Find each WBC.
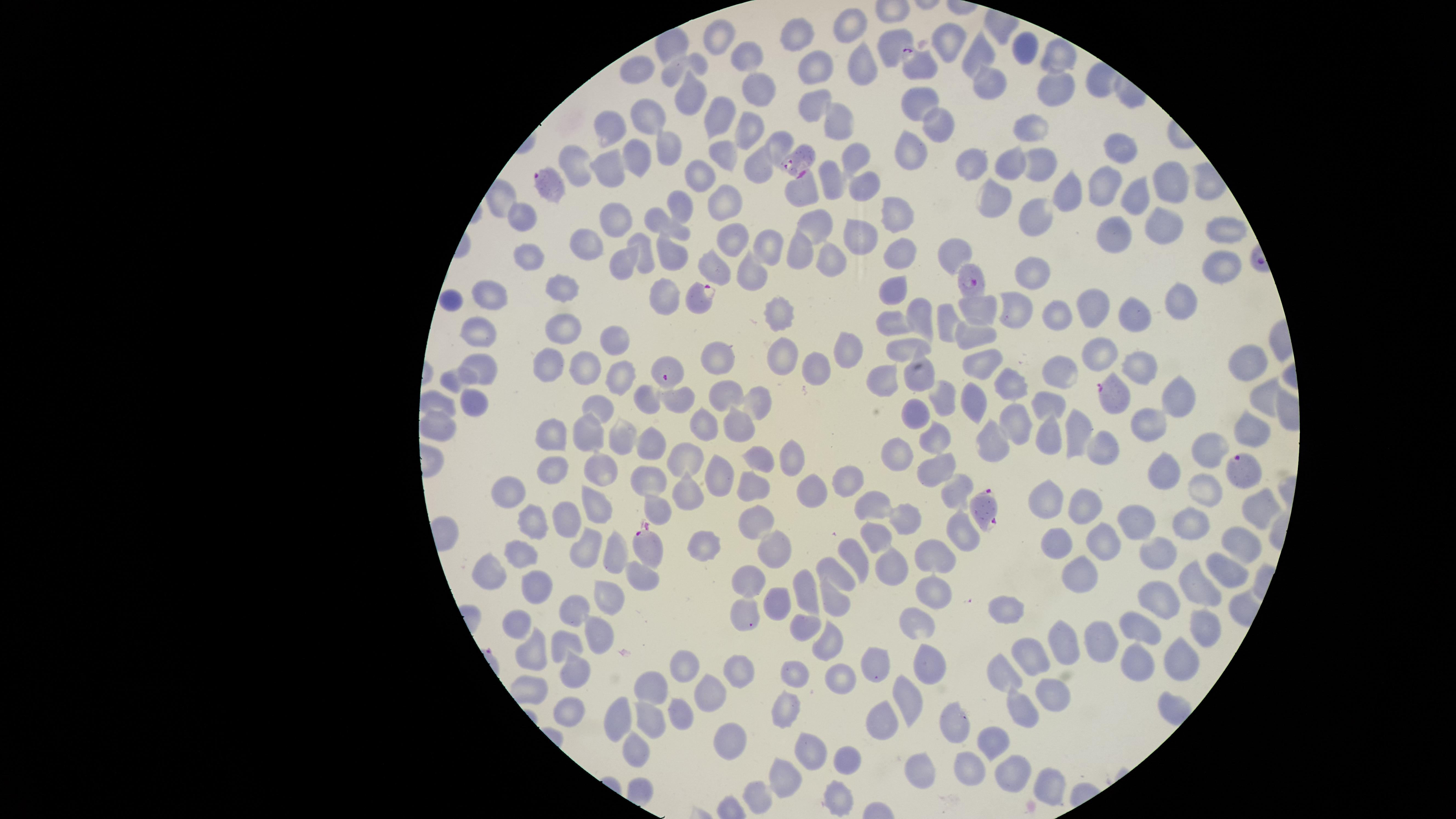
No WBCs identified.

image size = 1456×819 pixels
presence = malaria parasites identified
visible region = circular
stain = Giemsa
field of view = single
preparation = thin blood film
parasitized RBCs = approximate marker points as (x, y) in pixels: (924, 66), (799, 158), (549, 181), (966, 278), (698, 295), (665, 371), (1112, 393), (1242, 467), (985, 506), (645, 547)
uninfected RBCs = approximate marker points as (x, y) in pixels: (849, 25), (796, 30), (718, 35), (948, 37), (894, 39), (1017, 48), (978, 53), (1058, 53), (742, 56), (858, 62), (638, 70), (672, 72), (815, 72), (988, 84), (755, 89), (1055, 90), (690, 95), (920, 100), (810, 103), (645, 112), (715, 116), (838, 122), (933, 125), (748, 126), (611, 128), (1033, 131), (666, 143), (777, 144), (1118, 145), (911, 151), (721, 155), (633, 157), (856, 157), (1010, 161), (1039, 163), (973, 164), (580, 167), (611, 169), (756, 169), (699, 174), (831, 174), (1165, 180), (863, 185), (1103, 187), (802, 188), (1064, 194), (994, 198), (723, 199), (1132, 199), (680, 203), (896, 217), (523, 218), (1032, 219), (612, 225), (666, 226), (1160, 226), (818, 228), (1221, 228), (1109, 232), (732, 236), (857, 239), (769, 241), (586, 244), (795, 247), (642, 251), (899, 251), (672, 255), (954, 256), (528, 257), (827, 260), (714, 263), (625, 265), (1221, 267), (752, 273), (1030, 273), (566, 286), (892, 289), (493, 297), (451, 301), (665, 302), (1179, 303), (1092, 307), (780, 311), (978, 313), (1015, 313), (1133, 313), (921, 315), (1054, 315), (943, 321), (893, 323), (563, 328), (481, 332), (616, 333), (976, 334), (907, 347), (844, 349), (1097, 349), (783, 351), (717, 361), (819, 364), (550, 365), (1138, 365), (1247, 365), (585, 369), (981, 369), (1058, 369), (474, 372), (618, 376), (882, 378), (920, 378), (448, 380), (1003, 386), (726, 397), (942, 399), (1262, 399), (758, 400), (971, 400), (1176, 400), (643, 402), (676, 402), (1049, 403), (436, 404), (474, 410), (602, 410), (913, 416), (1016, 423), (1142, 423), (1078, 424), (697, 425), (436, 429), (741, 432), (1048, 432), (619, 433), (551, 435), (583, 435), (1248, 436), (939, 437), (650, 441), (1099, 442), (990, 445), (1201, 450), (792, 453), (897, 455), (683, 461), (762, 462), (601, 468), (557, 469), (1166, 470), (934, 472), (723, 473), (655, 480), (841, 480), (752, 487), (806, 487), (1204, 490), (505, 493), (688, 493), (956, 493), (1051, 497), (594, 503), (876, 503), (1080, 503), (657, 505), (1252, 507), (564, 515), (751, 515), (909, 518), (1137, 518), (1187, 525), (529, 527), (962, 535), (876, 537), (1059, 541), (1099, 541), (704, 542), (582, 543), (1240, 543), (775, 550), (1156, 551), (608, 554), (855, 556), (936, 557), (518, 560), (886, 565), (835, 570), (492, 571), (1223, 571), (643, 577), (1080, 577), (750, 579), (535, 586), (806, 587), (1196, 587), (930, 589), (609, 595), (833, 596), (1164, 599), (776, 603), (1007, 608), (579, 611), (745, 614), (1205, 624), (516, 627), (924, 627), (1142, 627), (604, 633), (566, 643), (1100, 643), (1064, 646), (821, 647), (1136, 653), (1032, 654), (536, 655), (1174, 656), (930, 657), (876, 665), (738, 669), (681, 671), (796, 672), (1005, 672), (576, 673), (839, 681), (652, 687), (710, 690), (1054, 693), (910, 695), (790, 707), (1017, 709), (570, 710), (681, 710), (616, 716), (643, 719), (885, 719), (952, 724), (738, 735), (990, 741), (633, 746), (812, 751), (847, 760), (969, 762), (923, 767), (1011, 769), (790, 776), (1048, 785), (834, 794), (758, 797)
capture = smartphone photograph through the microscope eyepiece
species = Plasmodium falciparum